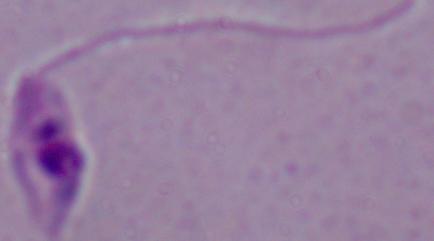
Summary:
  - Modality: micrograph
  - Magnification: 1000x
  - Identification: Leishmania